Report the malaria status of this cell.
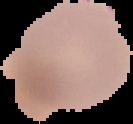
It is parasitized.

From a thin blood film. Image is 133×124 pixels. The area outside the segmented cell region is set to black.